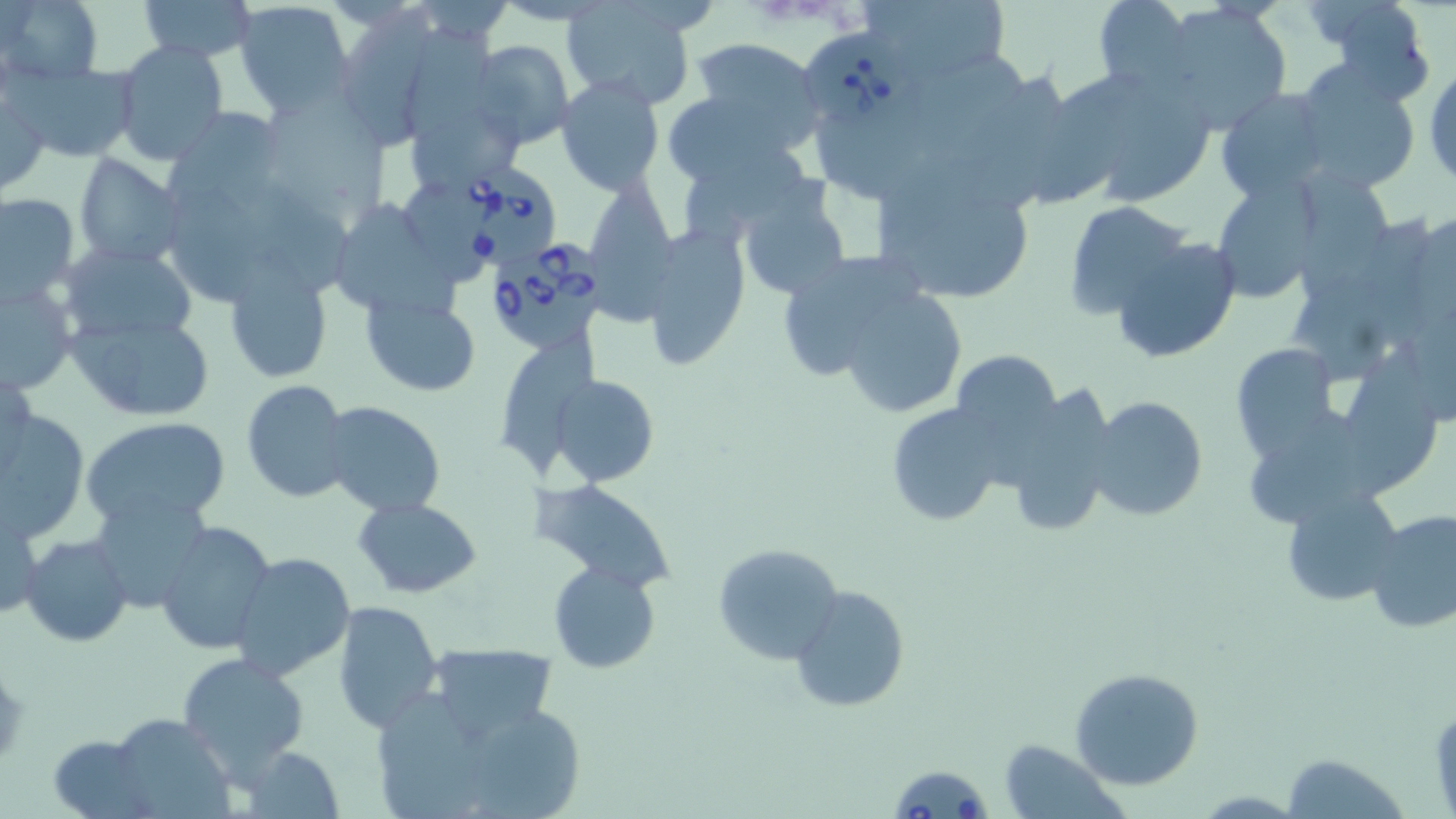
Approximate bounding boxes as (x1,y1)-(x2,y2) corner pairs in pixels. Uninfected red blood cell locations: (1,0)-(102,84), (138,0)-(257,60), (865,0)-(1012,90), (1093,0)-(1195,91), (234,1)-(356,114), (561,4)-(700,110), (1158,4)-(1291,134), (1330,4)-(1434,104), (333,10)-(439,150), (407,27)-(504,140), (686,37)-(823,152), (468,40)-(575,151), (115,42)-(229,166), (916,52)-(1029,165), (517,53)-(641,170), (10,62)-(139,163), (1426,63)-(1456,191), (1290,64)-(1422,194), (1064,68)-(1210,205), (961,73)-(1073,212), (555,75)-(667,198), (660,85)-(798,187), (1217,89)-(1330,203), (0,92)-(48,194), (270,97)-(386,219), (815,106)-(956,194), (162,108)-(287,212), (408,115)-(521,187), (683,150)-(811,245), (74,153)-(185,268), (868,158)-(1039,307), (1305,172)-(1399,296), (587,175)-(681,323), (1208,175)-(1325,305), (170,185)-(264,306), (735,187)-(850,303), (1,192)-(80,303), (326,196)-(459,312), (1062,200)-(1190,319), (643,222)-(752,371), (1109,236)-(1242,363), (61,245)-(198,347), (772,249)-(926,383), (222,264)-(336,384), (1285,272)-(1421,358), (0,275)-(78,398), (837,288)-(966,419), (361,295)-(480,396), (67,311)-(214,421), (1229,341)-(1341,458), (1340,343)-(1440,490), (951,348)-(1061,448), (1,357)-(34,475), (551,374)-(658,488), (240,379)-(353,504), (996,386)-(1117,539), (1085,394)-(1211,523), (320,401)-(448,518), (885,401)-(1008,529), (1245,405)-(1372,528), (1,407)-(89,543), (80,414)-(232,530), (535,480)-(675,593), (1281,484)-(1404,607), (90,493)-(212,615), (356,497)-(484,598), (1,500)-(44,623), (1367,503)-(1456,630), (155,520)-(276,656), (22,535)-(134,647), (713,541)-(844,668), (229,553)-(356,683), (549,561)-(661,674), (789,584)-(910,714), (332,600)-(444,732), (425,643)-(560,745), (176,650)-(309,779), (1070,667)-(1204,791), (377,687)-(476,781), (483,710)-(591,819), (103,711)-(235,818), (47,735)-(155,819), (998,738)-(1126,819), (237,744)-(347,819), (1280,753)-(1411,819). Babesia divergens-infected red blood cell locations: (803,28)-(917,128), (440,164)-(563,271), (489,242)-(614,350), (889,761)-(994,819). Slide-level diagnosis: Babesia divergens. Thin blood smear. May-Grünwald-Giemsa stain. Light microscopy. 1000x magnification. Single field of view. Image is 1456×819 pixels.